Report the malaria status of this cell.
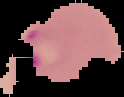

It is parasitized.

The area outside the segmented cell region is set to black. Image is 124×97 pixels. From a thin blood smear.